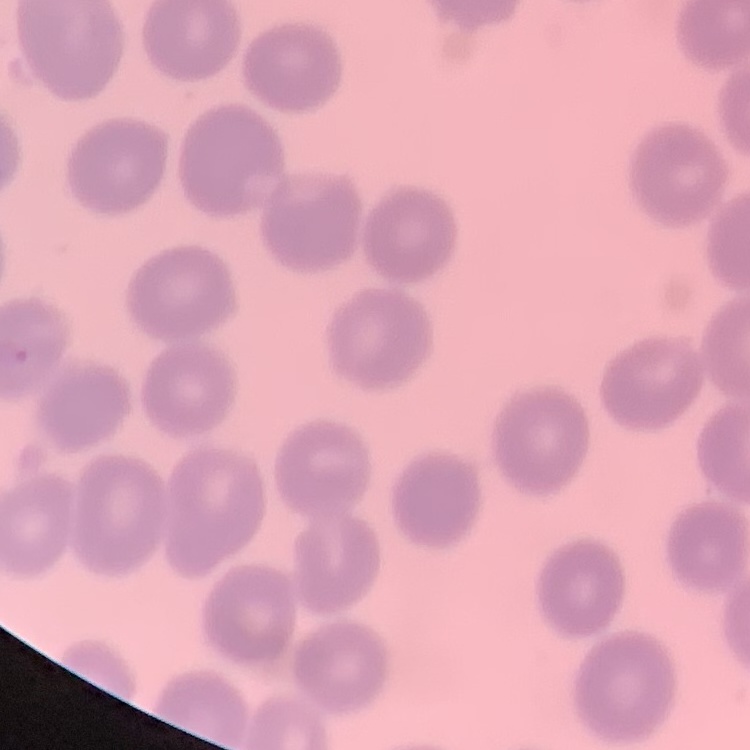
The erythrocytes show no rouleaux formation. Square crop of a larger photomicrograph. Stained with either Field's or Giemsa. Thin blood film.